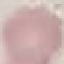

Malaria status: uninfected. Giemsa stain. Thin blood smear. Cell patch, automatically extracted from a larger field of view and resized to 64 × 64 pixels. Photographed with a smartphone camera at the microscope eyepiece.